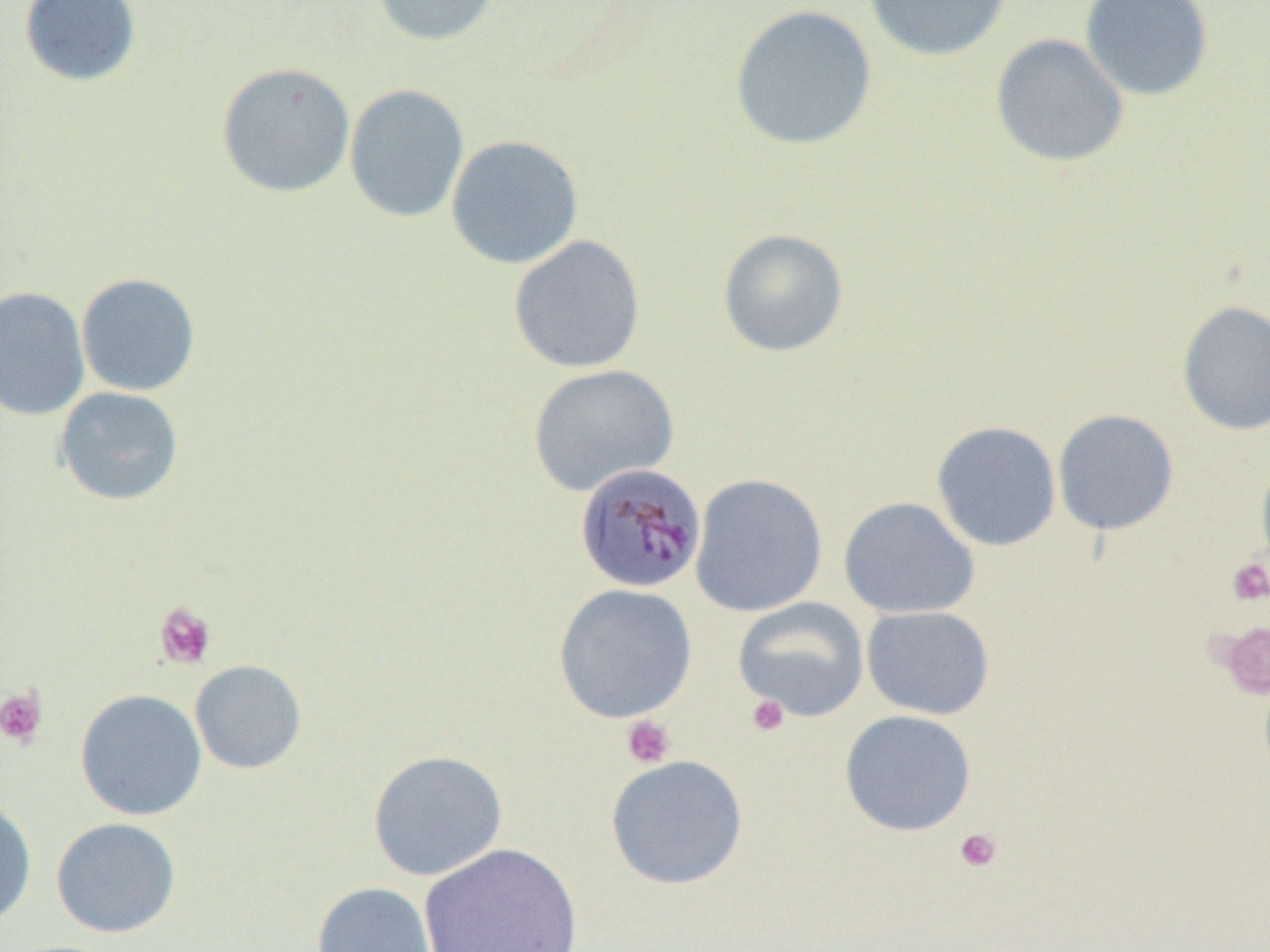
Approximate bounding boxes as named x1/y1/x2/y2 corners in pixels. Platelet locations (subset): (x1=1227, y1=558, x2=1269, y2=605), (x1=153, y1=602, x2=217, y2=669), (x1=0, y1=686, x2=48, y2=747), (x1=746, y1=694, x2=790, y2=737), (x1=621, y1=715, x2=676, y2=769), (x1=954, y1=827, x2=1002, y2=872). Plasmodium malariae-infected red blood cell locations: (x1=573, y1=462, x2=707, y2=594). Uninfected red blood cell locations (subset): (x1=19, y1=0, x2=142, y2=88), (x1=371, y1=0, x2=503, y2=46), (x1=864, y1=0, x2=1010, y2=61), (x1=1079, y1=0, x2=1214, y2=102), (x1=729, y1=5, x2=878, y2=151), (x1=990, y1=33, x2=1128, y2=167), (x1=216, y1=62, x2=356, y2=198), (x1=344, y1=83, x2=469, y2=223), (x1=445, y1=134, x2=584, y2=269), (x1=717, y1=228, x2=849, y2=357), (x1=508, y1=234, x2=646, y2=374), (x1=75, y1=272, x2=201, y2=397), (x1=0, y1=286, x2=90, y2=421), (x1=1176, y1=300, x2=1270, y2=436), (x1=527, y1=364, x2=679, y2=497), (x1=54, y1=386, x2=185, y2=506), (x1=1052, y1=408, x2=1179, y2=535), (x1=930, y1=420, x2=1062, y2=552), (x1=1255, y1=455, x2=1270, y2=578), (x1=690, y1=473, x2=828, y2=617), (x1=838, y1=496, x2=980, y2=619), (x1=553, y1=583, x2=698, y2=723), (x1=732, y1=597, x2=870, y2=722), (x1=861, y1=605, x2=995, y2=719), (x1=190, y1=659, x2=307, y2=774), (x1=74, y1=688, x2=207, y2=821), (x1=839, y1=709, x2=976, y2=837), (x1=367, y1=749, x2=508, y2=881), (x1=605, y1=754, x2=749, y2=890), (x1=0, y1=798, x2=37, y2=927), (x1=50, y1=816, x2=182, y2=938), (x1=418, y1=843, x2=583, y2=951), (x1=311, y1=882, x2=437, y2=952). Slide-level diagnosis: Plasmodium malariae. Optical microscopy. Captured at 1000x magnification. Thin blood film. Image is 1270×952 pixels. Single field of view.